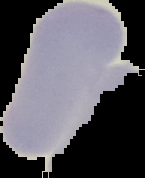

preparation: thin blood film
image_type: cell region segmented out of the field of view; surrounding area masked to black
result: negative for malaria parasites
image_size: 145×178 pixels